Locate every Plasmodium malariae-infected red blood cell.
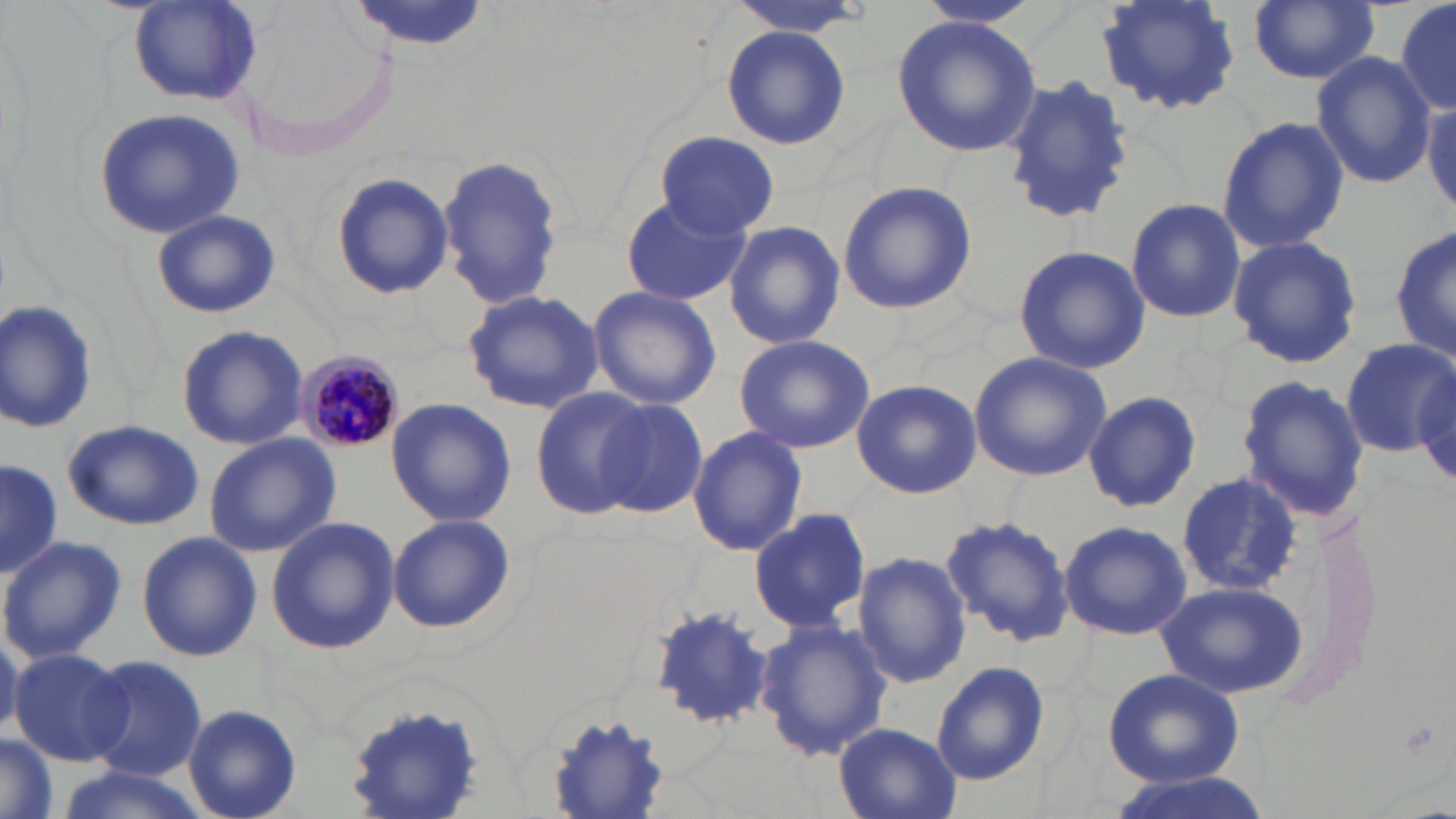
Approximate bounding boxes as (x1, y1, x2, y2) in pixels.
Plasmodium malariae-infected red blood cells: (296, 351, 402, 454).

slide_level_diagnosis: Plasmodium malariae
modality: optical microscopy
magnification: 1000x
stain: May-Grünwald-Giemsa
uninfected_red_blood_cell_locations: 'approximate bounding boxes as (x1, y1, x2, y2) in pixels: (346, 0, 488, 51), (727, 0, 877, 38), (915, 0, 1041, 29), (1096, 0, 1241, 116), (1248, 0, 1381, 85), (1391, 0, 1455, 118), (127, 1, 262, 107), (891, 16, 1042, 159), (722, 26, 850, 148), (1310, 51, 1434, 190), (999, 76, 1134, 224), (1423, 95, 1456, 220), (93, 108, 248, 237), (1215, 117, 1350, 253), (657, 130, 779, 238), (437, 154, 563, 311), (329, 172, 452, 299), (836, 180, 977, 315), (620, 192, 751, 307), (1125, 198, 1246, 322), (150, 209, 282, 319), (723, 221, 845, 352), (1391, 225, 1454, 366), (1228, 234, 1362, 368), (1013, 244, 1150, 375), (587, 286, 721, 409), (462, 289, 605, 417), (0, 297, 101, 435), (175, 323, 307, 451), (733, 335, 876, 454), (1342, 339, 1454, 458), (969, 352, 1112, 482), (1237, 375, 1365, 523), (851, 379, 982, 499), (529, 386, 659, 520), (1082, 389, 1202, 513), (593, 397, 708, 519), (385, 398, 515, 527), (63, 419, 205, 531), (687, 426, 807, 558), (204, 433, 340, 558), (0, 457, 60, 580), (1177, 469, 1304, 596), (747, 506, 871, 633), (941, 513, 1074, 648), (387, 515, 515, 633), (265, 517, 400, 654), (1059, 519, 1192, 641), (136, 532, 262, 661), (0, 535, 126, 665), (853, 551, 972, 688), (1154, 579, 1306, 699), (647, 607, 777, 728), (755, 618, 891, 762), (7, 647, 131, 765), (82, 655, 209, 780), (931, 660, 1050, 786), (1102, 668, 1244, 788), (346, 700, 487, 818), (182, 703, 303, 819), (545, 711, 673, 815), (835, 722, 963, 819), (0, 735, 58, 819), (49, 766, 213, 819), (1102, 768, 1279, 819)'
preparation: thin blood smear
image_size: 1456×819 pixels
field_of_view: single